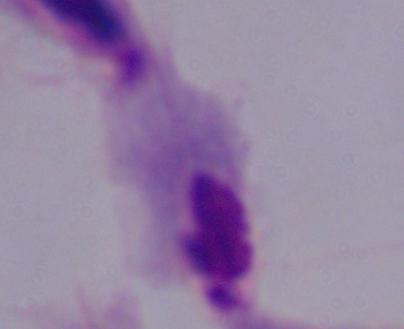

A trichomonad is shown. 1000x magnification. Micrograph.